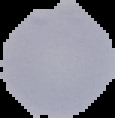 From a thin blood film. Result: malaria parasites identified. Cell region segmented out of the field of view; the surrounding area is masked to black. Image is 115×118 pixels.